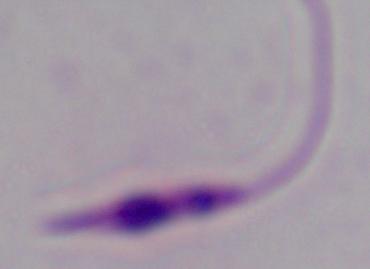

{
  "magnification": "1000x",
  "modality": "micrograph",
  "identification": "Leishmania"
}